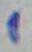

identification = Toxoplasma gondii
magnification = 1000x
modality = micrograph